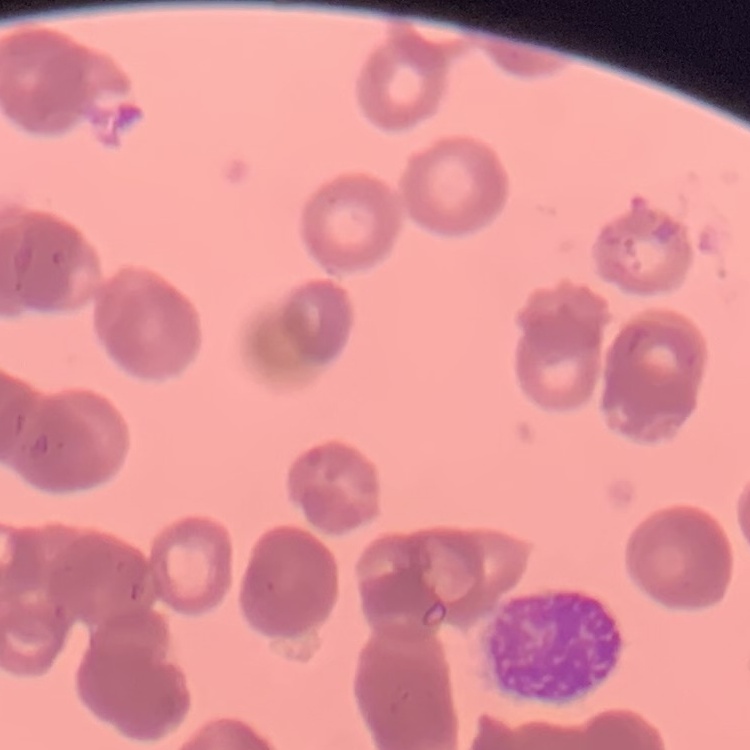 The red blood cells exhibit rouleaux formation. Field's or Giemsa stain. Square crop of a larger photomicrograph. Thin blood smear.